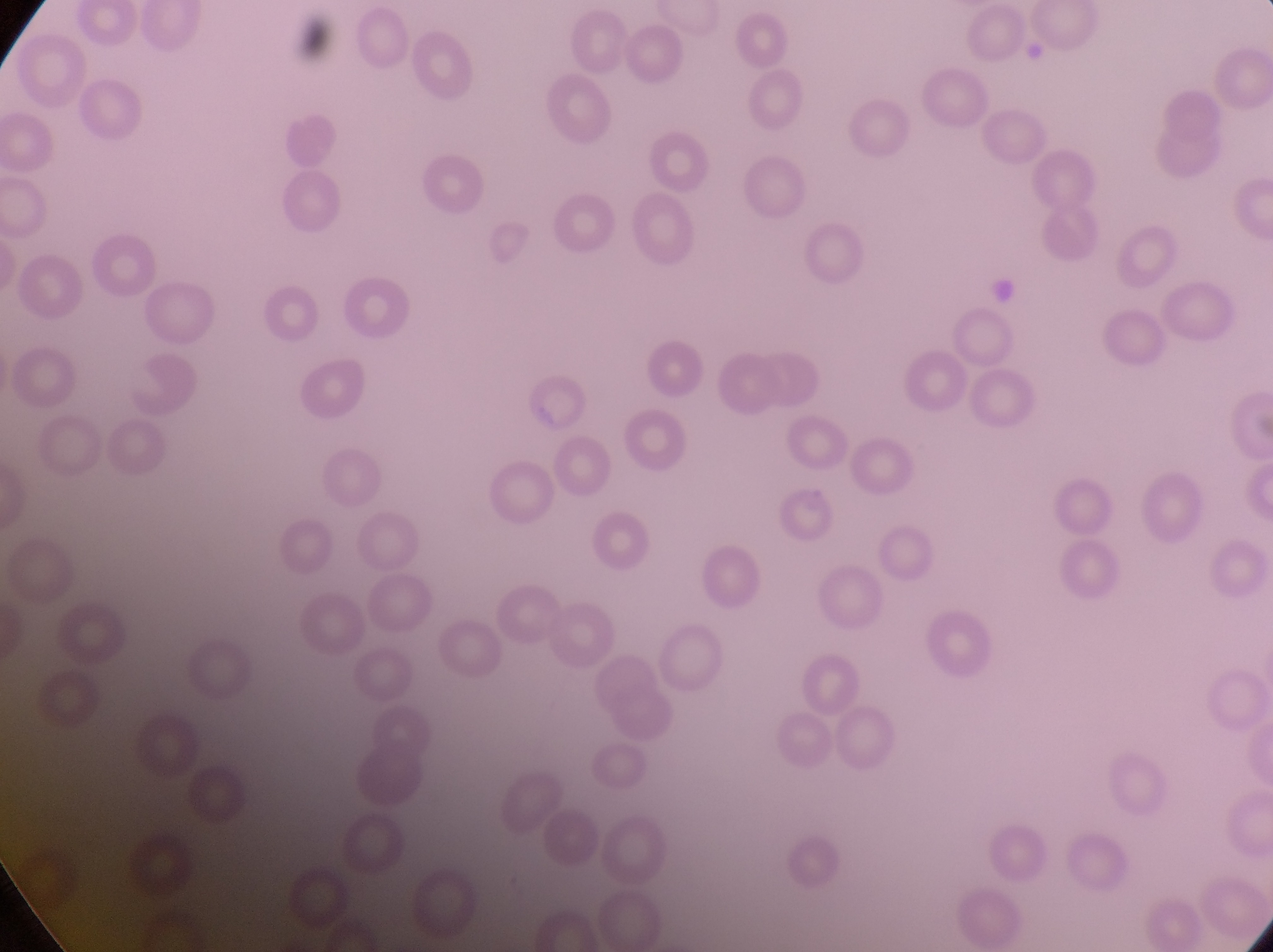
{
  "country": "Uganda",
  "image_size": "1273×952 pixels",
  "field_of_view": "single",
  "magnification": "1000x",
  "capture": "smartphone photograph through the eyepiece of an Olympus CX-23 microscope",
  "preparation": "thin blood smear",
  "parasitised_red_blood_cell_locations": "approximate bounding boxes as (left, top, right, bottom) in pixels: (784, 484, 837, 549)"
}